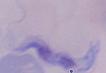

modality = micrograph
identification = trypanosome
magnification = 1000x